Comment on the morphology of the erythrocytes.
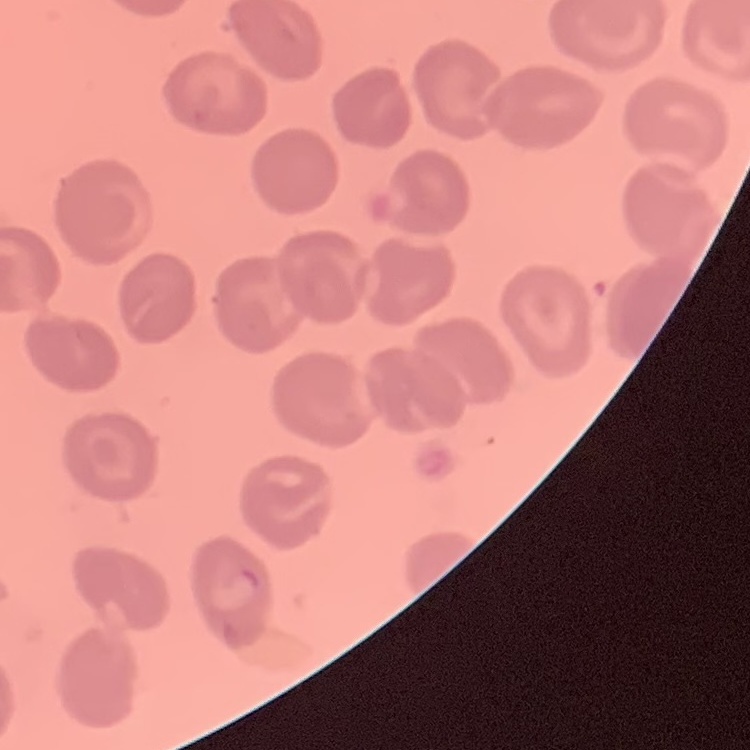

They show no rouleaux formation.

{
  "preparation": "thin peripheral smear",
  "image_type": "square crop of a larger photomicrograph",
  "stain": "Field's or Giemsa"
}